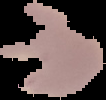

result = malaria parasites identified
image size = 106×100 pixels
preparation = thin blood film
image type = segmented cell region with the area outside set to black